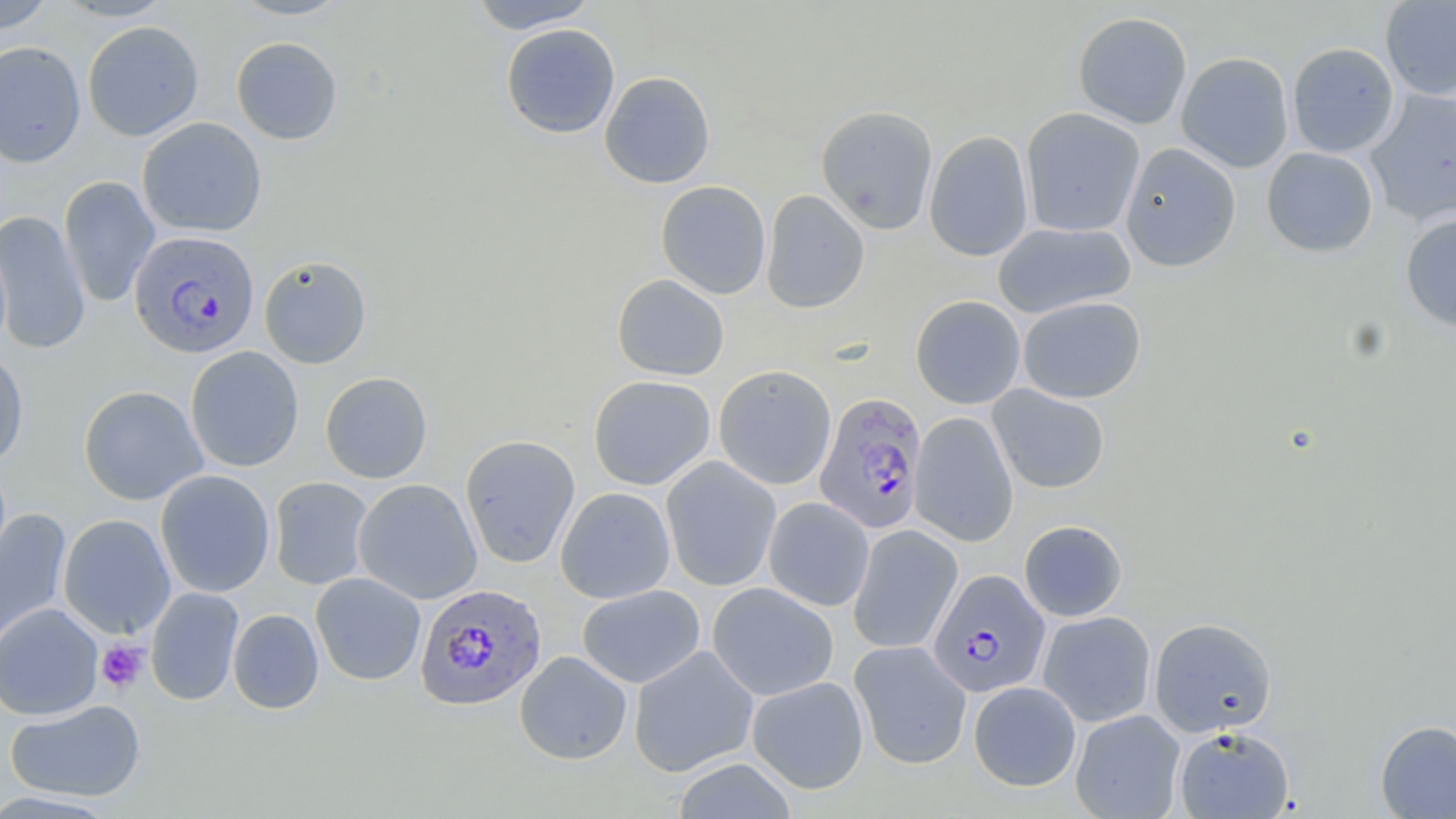

Summary:
  - Coordinate format: approximate bounding boxes as [x1, y1, x2, y2] in pixels
  - Plasmodium falciparum-infected red blood cell locations: [128, 230, 260, 359], [814, 392, 927, 535], [928, 569, 1050, 697], [415, 583, 547, 710]
  - Platelet locations: [96, 640, 148, 693]
  - Uninfected red blood cell locations: [53, 0, 175, 21], [228, 0, 354, 20], [467, 0, 600, 32], [1380, 0, 1456, 100], [0, 1, 55, 34], [1072, 11, 1193, 129], [82, 21, 204, 140], [500, 23, 620, 139], [231, 37, 343, 144], [0, 41, 86, 168], [1287, 42, 1399, 157], [1176, 52, 1294, 172], [599, 71, 716, 188], [1365, 89, 1456, 227], [816, 105, 938, 235], [1021, 107, 1145, 238], [137, 117, 267, 237], [924, 131, 1033, 261], [1119, 143, 1241, 272], [1261, 147, 1379, 257], [59, 176, 160, 307], [656, 180, 771, 299], [760, 189, 869, 314], [0, 210, 91, 356], [1400, 212, 1456, 333], [992, 221, 1136, 319], [259, 255, 372, 368], [612, 274, 729, 380], [910, 295, 1026, 409], [1018, 295, 1146, 404], [185, 346, 304, 472], [0, 350, 29, 469], [714, 365, 836, 489], [320, 372, 433, 483], [588, 375, 716, 490], [78, 385, 208, 505], [988, 385, 1110, 493], [910, 413, 1018, 546], [460, 434, 580, 568], [661, 456, 781, 591], [155, 469, 276, 597], [269, 477, 374, 590], [353, 479, 483, 604], [555, 486, 675, 604], [764, 498, 874, 611], [0, 507, 72, 649], [58, 513, 176, 639], [1019, 520, 1128, 622], [848, 524, 963, 654], [310, 572, 426, 685], [707, 582, 838, 701], [577, 584, 705, 688], [145, 587, 244, 706], [0, 602, 104, 720], [228, 609, 324, 714], [1038, 611, 1156, 727], [1149, 617, 1277, 737], [849, 640, 971, 769], [629, 645, 759, 777], [515, 650, 632, 765], [747, 676, 869, 794], [968, 681, 1081, 791], [5, 699, 146, 802], [1070, 709, 1185, 819], [1375, 720, 1456, 818], [1174, 726, 1294, 818], [671, 759, 797, 818]
  - Slide-level diagnosis: Plasmodium falciparum
  - Modality: light microscopy
  - Image size: 1456×819 pixels
  - Field of view: one of a larger specimen
  - Preparation: thin blood smear
  - Stain: May-Grünwald-Giemsa
  - Magnification: 1000x